Report the malaria status of this cell.
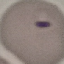
It is parasitized.

Summary:
  - Capture: smartphone camera at the microscope eyepiece
  - Image type: cell patch, automatically extracted from a larger field of view and resized to 64 × 64 pixels
  - Preparation: thin blood smear
  - Stain: Giemsa